Point out each Plasmodium parasite.
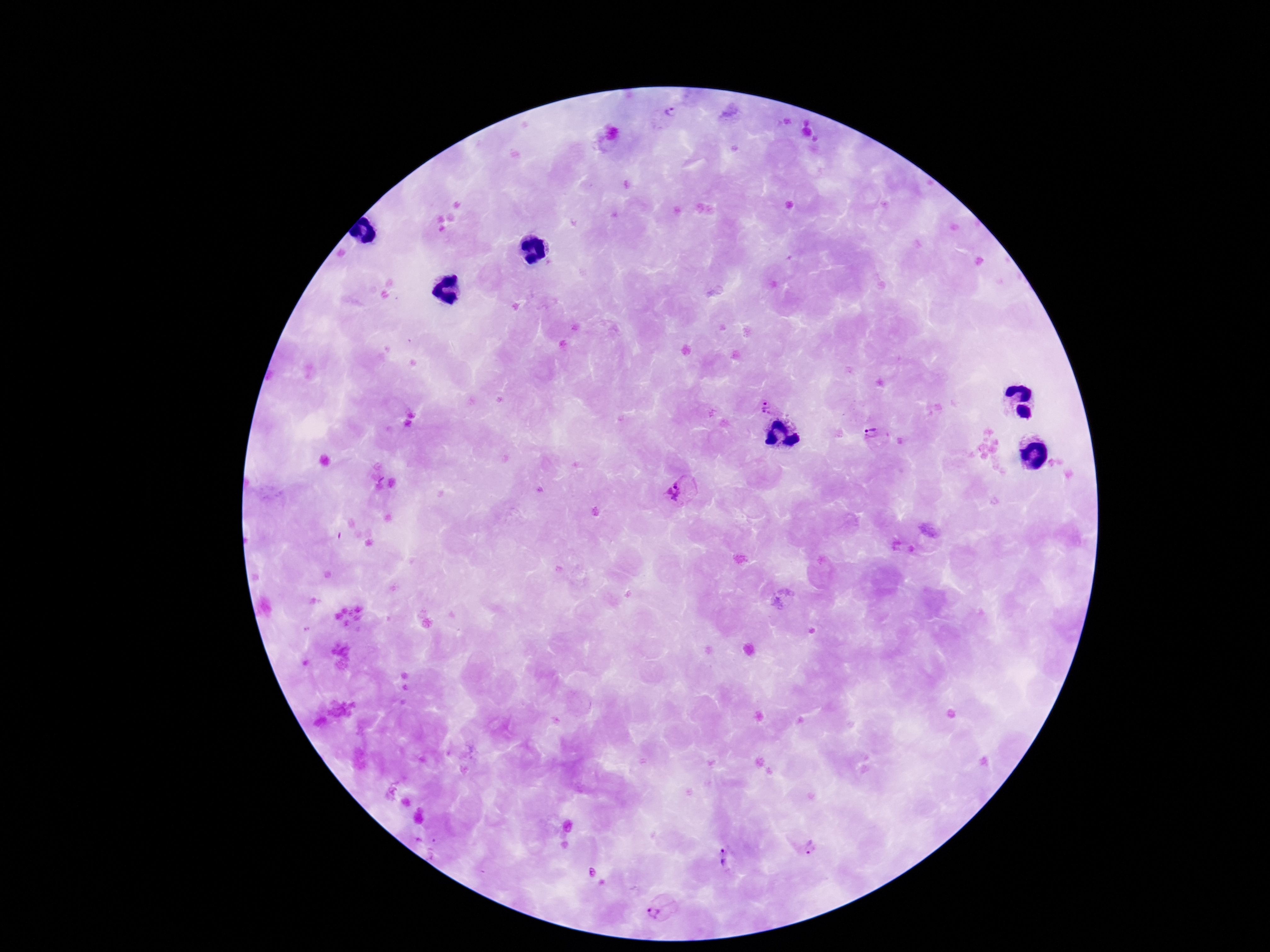
Approximate object centers, in pixels from the top-left corner.
Plasmodium parasites: (x=666, y=116), (x=769, y=406), (x=873, y=434), (x=678, y=490), (x=809, y=846), (x=724, y=859), (x=657, y=907).

Smartphone photograph taken through the microscope eyepiece. 100x magnification. Patient malaria status: positive. Single field of view. Image is 1270×952 pixels. Giemsa-stained preparation. Thick blood film.